Identify the blood parasite species.
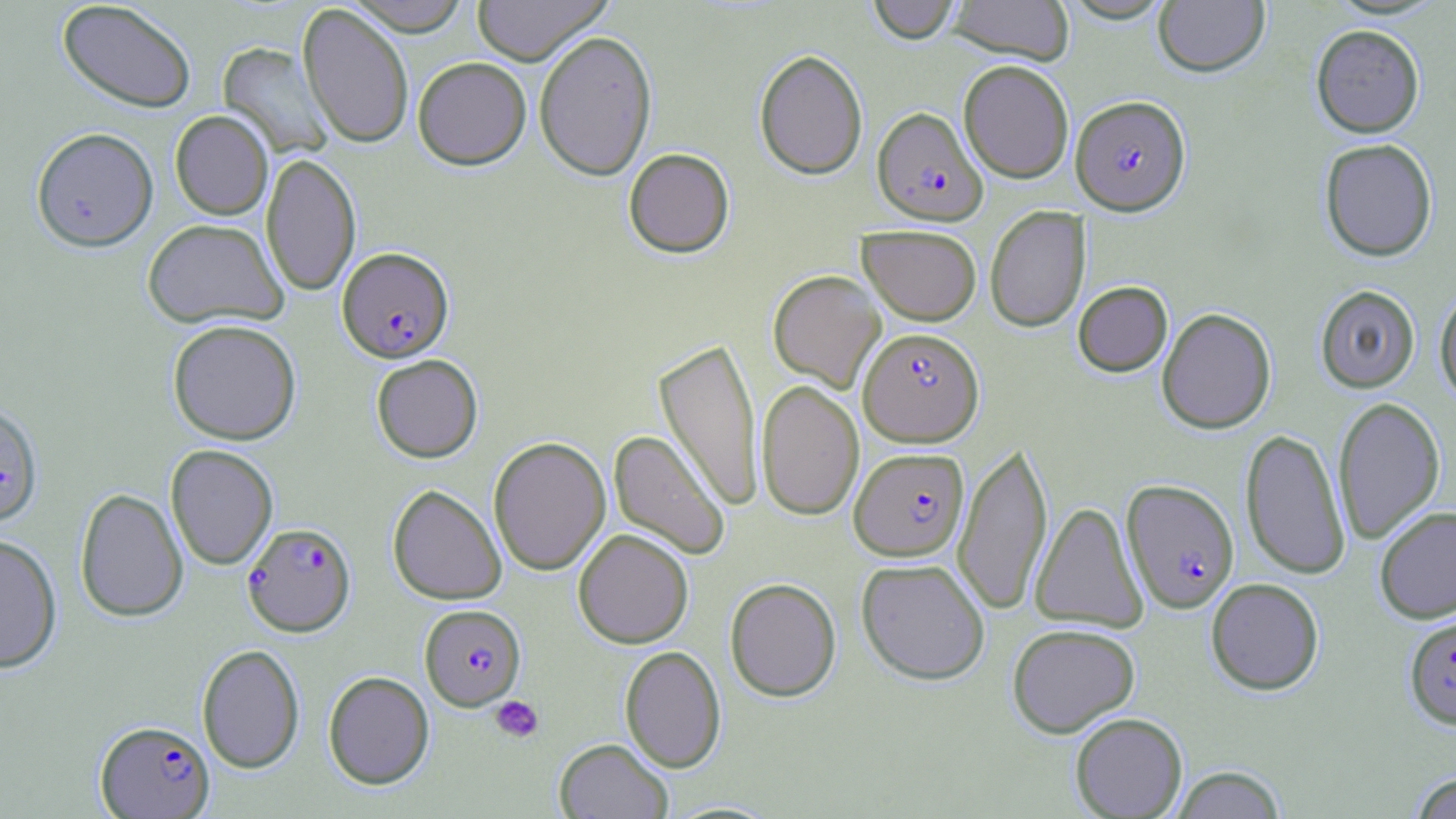

Plasmodium falciparum.

Summary:
  - Coordinate format: approximate bounding boxes as [x1, y1, x2, y2] in pixels
  - Plasmodium falciparum-infected red blood cell locations: [1071, 94, 1191, 215], [872, 107, 987, 225], [337, 247, 454, 362], [852, 330, 977, 449], [0, 402, 44, 527], [850, 447, 969, 561], [1122, 478, 1239, 613], [243, 521, 356, 636], [420, 604, 526, 710], [1404, 615, 1456, 729], [95, 720, 215, 818]
  - Platelet locations: [490, 695, 544, 743]
  - Uninfected red blood cell locations: [57, 0, 196, 113], [344, 0, 472, 36], [471, 0, 613, 66], [867, 0, 961, 44], [947, 0, 1075, 64], [1154, 0, 1270, 77], [297, 3, 414, 149], [1311, 24, 1424, 138], [534, 30, 658, 181], [217, 42, 333, 160], [754, 49, 868, 180], [413, 56, 531, 169], [958, 59, 1074, 184], [170, 110, 273, 220], [31, 127, 158, 251], [1319, 138, 1437, 261], [623, 148, 734, 258], [261, 153, 361, 297], [985, 206, 1091, 332], [143, 218, 288, 329], [858, 224, 982, 325], [768, 270, 886, 393], [1073, 281, 1173, 377], [1314, 284, 1420, 393], [1435, 287, 1456, 406], [1156, 307, 1276, 434], [167, 319, 302, 445], [654, 337, 764, 513], [371, 354, 483, 463], [756, 379, 864, 521], [1332, 396, 1445, 545], [1240, 428, 1351, 580], [608, 430, 730, 560], [488, 436, 611, 575], [953, 439, 1053, 616], [165, 444, 278, 570], [387, 484, 507, 604], [75, 487, 188, 623], [1030, 501, 1148, 632], [1374, 505, 1456, 623], [573, 529, 693, 648], [0, 533, 63, 673], [856, 558, 990, 685], [725, 577, 841, 702], [1206, 577, 1325, 695], [1006, 623, 1140, 738], [196, 643, 305, 773], [620, 645, 726, 773], [323, 671, 434, 789], [1069, 712, 1187, 818], [553, 737, 673, 818], [1169, 765, 1288, 818], [1409, 772, 1456, 818]
  - Magnification: 1000x
  - Preparation: thin blood film
  - Stain: May-Grünwald-Giemsa
  - Modality: optical microscopy
  - Field of view: one of a larger specimen
  - Image size: 1456×819 pixels